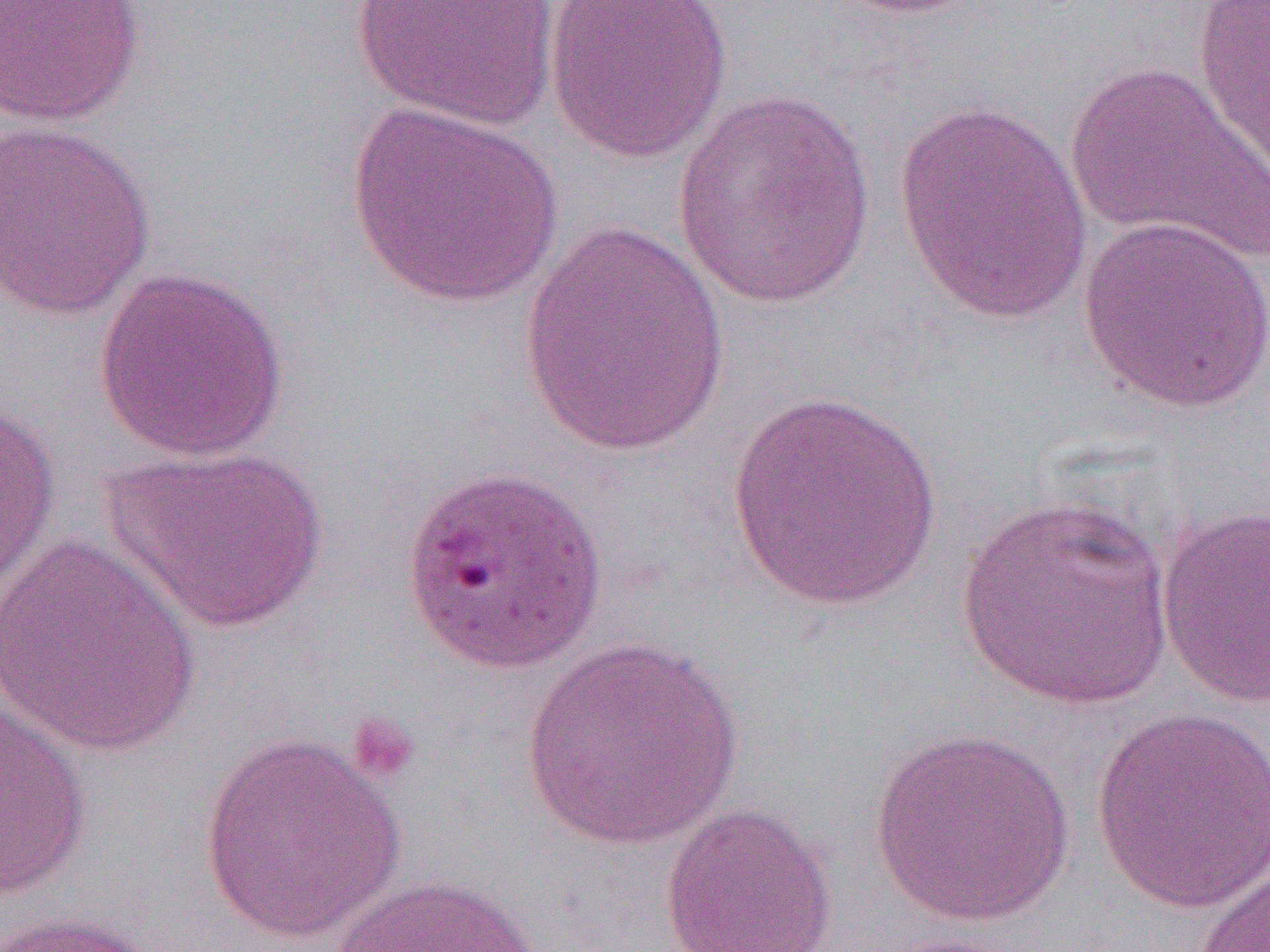

slide_level_diagnosis: Plasmodium falciparum
magnification: 1000x
modality: light microscopy
platelet_locations: 'approximate bounding boxes as (x1,y1)-(x2,y2) corner pairs in pixels: (345,712)-(421,787)'
image_size: 1270×952 pixels
field_of_view: one of a larger specimen
preparation: thin blood film
uninfected_red_blood_cell_locations: 'approximate bounding boxes as (x1,y1)-(x2,y2) corner pairs in pixels: (351,0)-(563,132), (543,0)-(735,164), (827,0)-(994,20), (1191,0)-(1270,191), (0,1)-(145,127), (1064,61)-(1270,266), (672,88)-(877,310), (893,97)-(1096,323), (344,101)-(566,310), (1,118)-(157,321), (1077,214)-(1270,414), (520,223)-(733,457), (93,264)-(292,461), (723,388)-(946,612), (0,403)-(61,601), (101,444)-(330,635), (954,494)-(1176,709), (1155,506)-(1269,710), (0,536)-(206,760), (520,638)-(742,851), (0,698)-(92,901), (1091,706)-(1270,913), (868,726)-(1077,927), (199,731)-(406,945), (659,802)-(838,952), (1189,854)-(1269,951), (329,872)-(543,952), (0,910)-(166,952), (870,932)-(1026,952)'